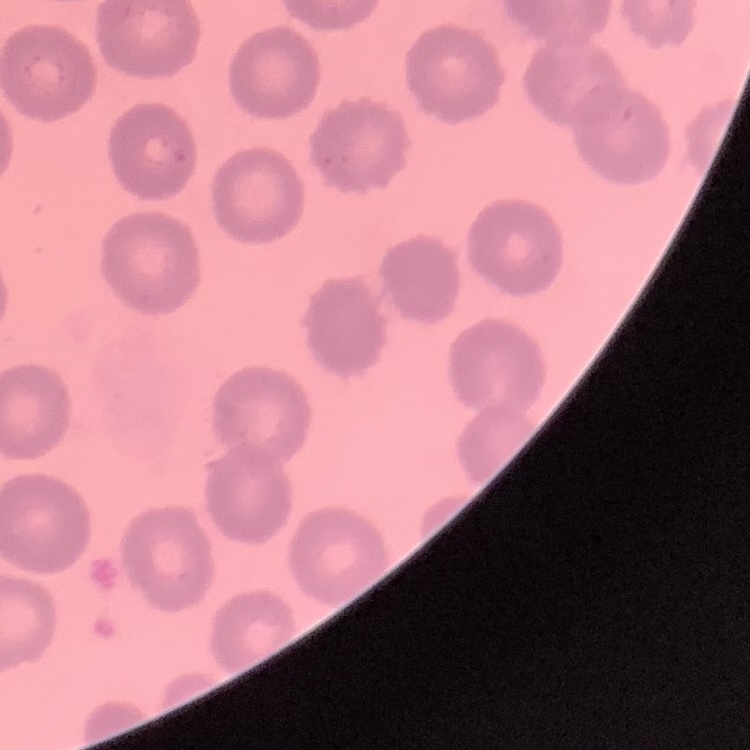
Summary:
  - Red blood cell morphology: no rouleaux formation
  - Image type: one tile cut from a larger photomicrograph
  - Stain: Field's or Giemsa
  - Preparation: thin blood smear